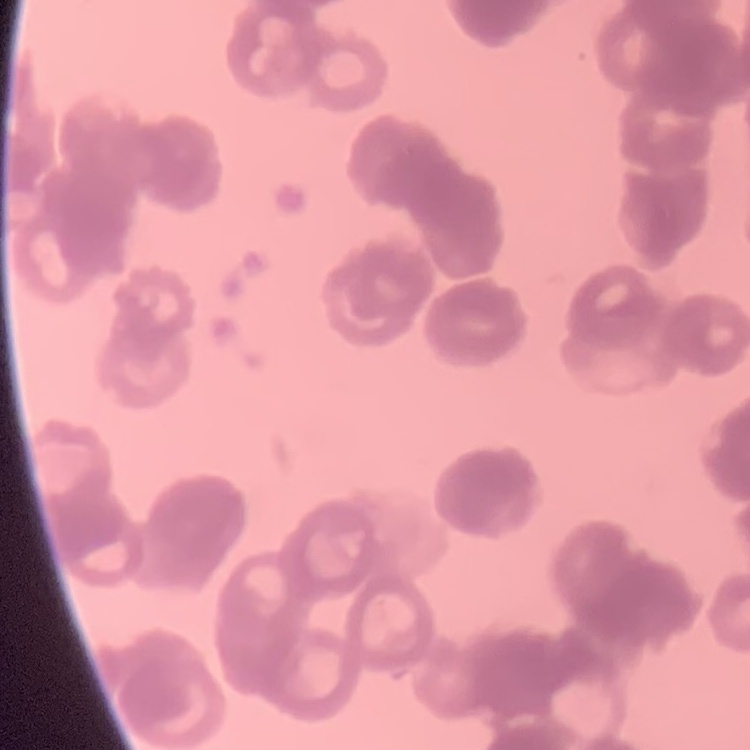

Summary:
  - Erythrocyte morphology: rouleaux formation
  - Image type: one tile cut from a larger photomicrograph
  - Stain: Field's or Giemsa
  - Preparation: thin blood smear